Report the malaria status of this cell.
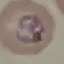

It is parasitized.

Summary:
  - Stain: Giemsa
  - Image type: automatically extracted cell patch, resized to 64 × 64 pixels
  - Capture: smartphone camera at the microscope eyepiece
  - Preparation: thin smear